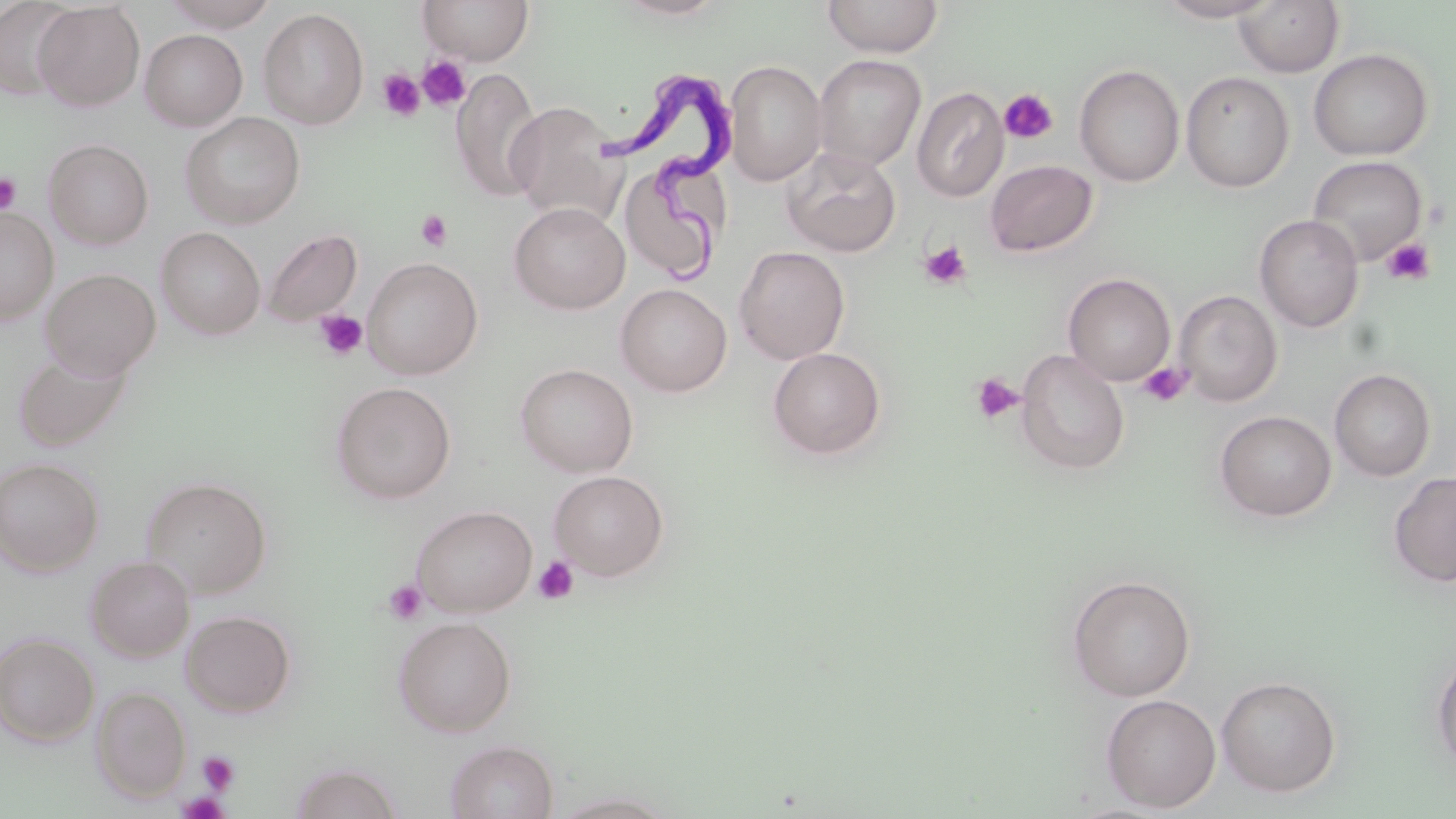
Summary:
  - Coordinate format: approximate bounding boxes as (x1,y1)-(x2,y2) corner pairs in pixels
  - Trypanosoma brucei locations: (610,76)-(744,279)
  - Uninfected red blood cell locations: (0,0)-(78,101), (160,0)-(280,30), (419,0)-(533,65), (608,0)-(733,21), (822,0)-(944,58), (1158,0)-(1280,22), (1234,1)-(1345,77), (33,2)-(145,111), (258,8)-(369,128), (137,21)-(369,127), (139,29)-(247,131), (1308,48)-(1433,160), (812,54)-(926,171), (724,59)-(827,186), (1074,64)-(1185,187), (451,67)-(543,201), (1180,71)-(1295,192), (911,87)-(1008,202), (505,101)-(625,224), (180,112)-(305,229), (43,139)-(154,250), (782,147)-(901,256), (617,154)-(731,285), (1307,155)-(1428,266), (984,159)-(1097,257), (509,202)-(630,314), (0,208)-(58,323), (1254,214)-(1364,333), (156,227)-(265,339), (262,229)-(362,326), (734,246)-(850,364), (362,257)-(483,379), (40,268)-(161,380), (1063,273)-(1176,385), (615,283)-(732,396), (1174,290)-(1282,406), (12,347)-(133,453), (767,347)-(887,461), (1015,349)-(1129,475), (515,363)-(638,477), (1330,368)-(1436,481), (331,382)-(456,504), (1215,410)-(1337,521), (0,457)-(103,575), (548,470)-(670,581), (1389,471)-(1456,588), (140,476)-(272,597), (411,505)-(537,616), (86,555)-(194,662), (1067,574)-(1196,702), (180,610)-(296,717), (393,616)-(517,736), (0,632)-(100,746), (1431,647)-(1456,774), (1215,675)-(1342,797), (92,685)-(191,801), (1100,693)-(1221,813), (445,739)-(558,819), (289,762)-(404,819), (551,791)-(676,817)
  - Platelet locations: (418,55)-(472,111), (377,69)-(425,120), (999,88)-(1058,144), (0,172)-(22,215), (416,209)-(453,252), (1381,238)-(1436,286), (919,239)-(973,290), (313,309)-(368,362), (1138,362)-(1192,407), (970,373)-(1023,425), (532,556)-(579,605), (382,579)-(428,624), (197,751)-(239,795), (176,792)-(230,818)
  - Slide-level diagnosis: Trypanosoma brucei
  - Preparation: thin blood film
  - Image size: 1456×819 pixels
  - Field of view: single
  - Modality: optical microscopy
  - Magnification: 1000x
  - Stain: May-Grünwald-Giemsa